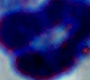

Captured at 1000x magnification. A leukocyte is seen. Micrograph.